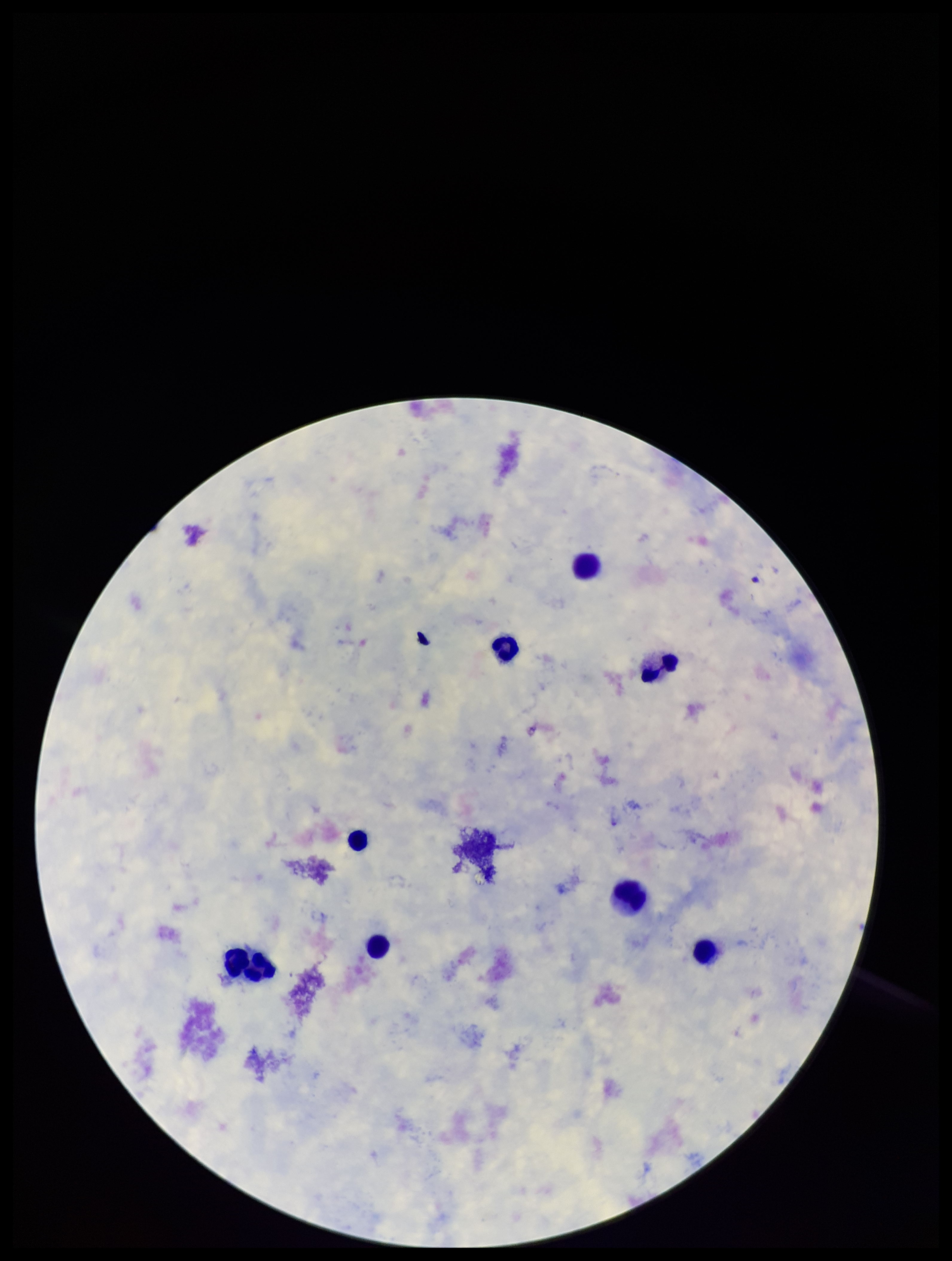 One field from this slide. Leukocyte count: 8. Plasmodium parasites: none seen. Smartphone photograph taken through the eyepiece of a microscope. Patient malaria status: negative. Preparation: thick blood smear. Giemsa stain. Image is 952×1261 pixels. Parasite count: 0.